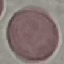

Summary:
  - Malaria status: uninfected
  - Image type: cell patch, automatically extracted from a larger field of view and resized to 64 × 64 pixels
  - Stain: Giemsa
  - Capture: smartphone through the microscope eyepiece
  - Preparation: thin blood smear